Classify this cell by malaria status.
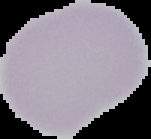

Uninfected.

preparation = thin blood smear
image size = 151×139 pixels
image type = cell region segmented out of the field of view; surrounding area masked to black